Report the malaria status of this cell.
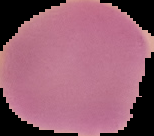

Uninfected.

image_size: 154×136 pixels
image_type: cell region segmented out of the field of view; surrounding area masked to black
preparation: thin blood smear